Report the malaria status of this cell.
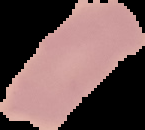

It is uninfected.

Image is 145×130 pixels. Segmented cell region on a black background. From a thin blood film.